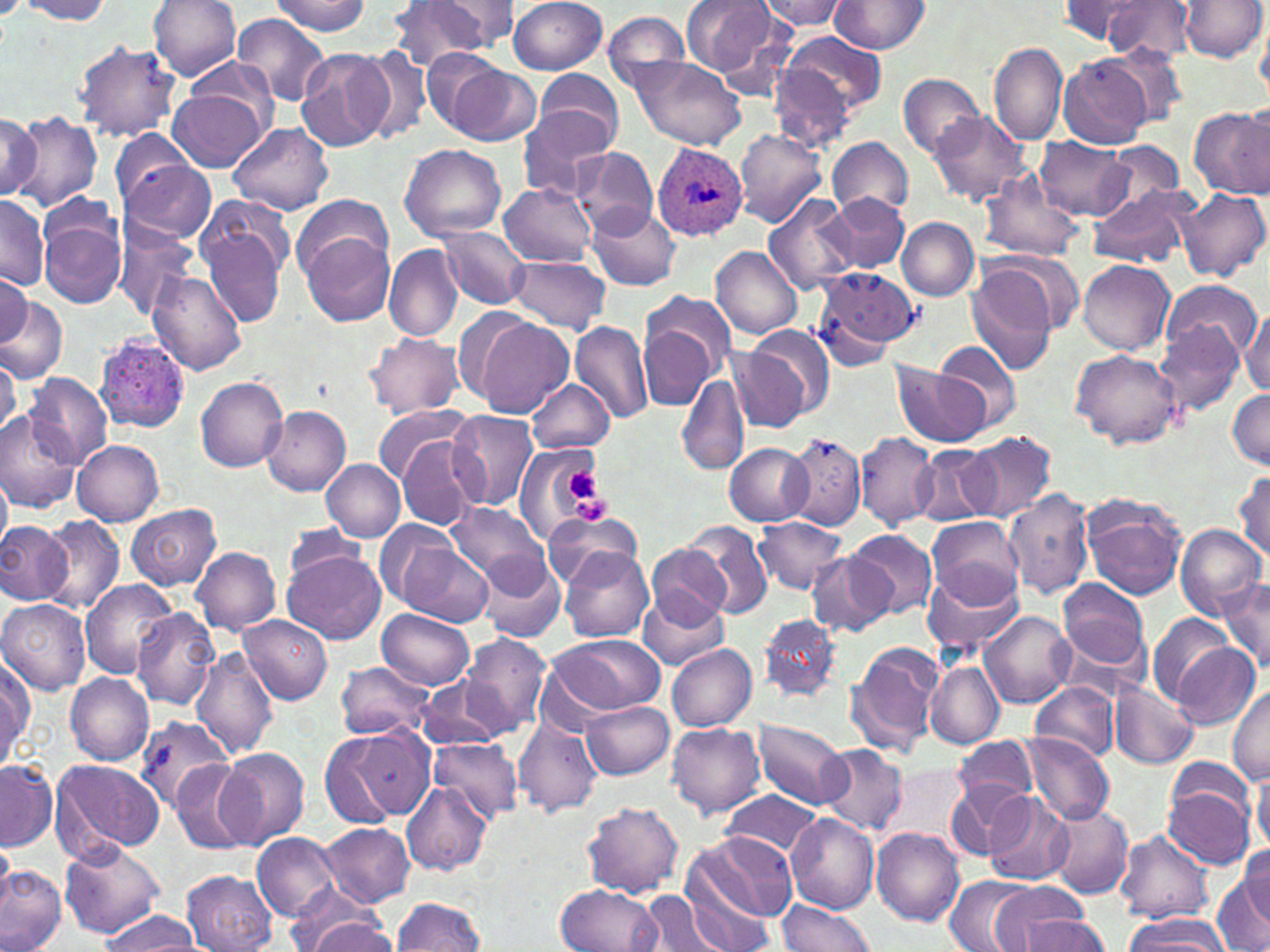
Summary:
  - Coordinate format: approximate bounding boxes as (x1,y1)-(x2,y2) corner pairs in pixels
  - Platelet locations: (564,467)-(612,524)
  - Plasmodium ovale-infected red blood cell locations: (652,143)-(749,240)
  - Uninfected red blood cell locations: (148,0)-(242,81), (272,0)-(372,36), (508,0)-(608,75), (681,0)-(780,79), (830,0)-(929,54), (1103,0)-(1195,64), (1179,0)-(1265,63), (18,1)-(116,25), (757,1)-(850,30), (1055,1)-(1151,47), (386,2)-(494,75), (428,2)-(520,52), (601,9)-(692,94), (233,13)-(330,106), (1256,17)-(1270,102), (257,26)-(366,129), (779,31)-(886,118), (74,41)-(182,143), (989,43)-(1068,148), (1100,43)-(1190,129), (353,45)-(434,146), (295,47)-(391,152), (417,47)-(507,133), (183,56)-(280,133), (632,56)-(747,150), (1059,56)-(1151,149), (439,60)-(539,145), (769,61)-(860,152), (535,69)-(624,151), (898,73)-(984,160), (168,89)-(268,172), (1236,101)-(1268,193), (521,106)-(618,199), (1189,106)-(1270,197), (929,110)-(1032,209), (7,111)-(103,213), (0,113)-(40,199), (229,122)-(334,215), (107,128)-(201,211), (735,128)-(828,227), (828,136)-(913,220), (1037,137)-(1134,222), (1102,142)-(1185,213), (398,143)-(508,240), (570,147)-(658,234), (117,158)-(217,245), (978,174)-(1086,264), (498,183)-(598,267), (1176,186)-(1269,282), (1089,187)-(1196,268), (763,193)-(860,296), (0,194)-(51,291), (293,194)-(393,274), (828,194)-(909,273), (587,204)-(680,291), (196,206)-(293,331), (39,212)-(126,310), (897,218)-(978,301), (111,224)-(199,321), (437,225)-(532,309), (300,231)-(395,327), (383,242)-(464,342), (712,246)-(804,339), (982,252)-(1082,339), (508,255)-(611,334), (1077,260)-(1175,355), (813,266)-(921,361), (966,266)-(1056,375), (147,270)-(247,375), (0,273)-(31,346), (1159,279)-(1262,364), (642,290)-(737,385), (0,296)-(67,383), (1241,307)-(1270,399), (468,313)-(574,418), (640,319)-(718,411), (1153,319)-(1245,416), (569,322)-(654,424), (364,331)-(462,418), (727,332)-(825,433), (94,336)-(189,434), (936,340)-(1022,431), (1071,349)-(1181,449), (892,363)-(989,448), (26,373)-(114,469), (676,373)-(748,474), (197,376)-(289,472), (528,380)-(613,453), (1228,388)-(1270,469), (372,405)-(469,484), (262,406)-(351,496), (0,411)-(81,512), (446,411)-(538,512), (963,431)-(1058,521), (855,432)-(940,533), (395,433)-(484,532), (785,434)-(867,529), (73,440)-(164,526), (725,443)-(814,526), (910,444)-(998,526), (515,445)-(612,543), (321,459)-(405,542), (1232,469)-(1270,566), (0,470)-(11,560), (1005,488)-(1095,600), (1079,496)-(1188,600), (447,503)-(551,589), (126,504)-(221,591), (541,512)-(644,588), (40,514)-(125,615), (927,515)-(1024,608), (753,516)-(849,594), (375,519)-(465,614), (0,520)-(72,606), (685,520)-(772,619), (282,522)-(373,593), (1176,525)-(1266,618), (846,529)-(938,619), (646,545)-(733,626), (399,546)-(495,629), (190,547)-(281,635), (559,548)-(656,642), (283,550)-(385,643), (806,552)-(892,636), (476,554)-(566,643), (922,566)-(1026,657), (1057,577)-(1151,675), (1218,578)-(1270,676), (80,579)-(179,678), (636,594)-(731,671), (0,598)-(91,693), (129,609)-(221,709), (378,609)-(476,690), (981,610)-(1076,709), (758,613)-(842,705), (1147,614)-(1236,705), (237,615)-(332,704), (458,632)-(552,736), (540,634)-(666,720), (844,641)-(944,757), (1167,641)-(1260,729), (666,642)-(757,732), (192,648)-(276,760), (0,650)-(34,766), (925,661)-(1004,748), (333,662)-(436,739), (64,672)-(154,766), (416,678)-(508,751), (1029,680)-(1122,764), (1110,681)-(1198,770), (1229,687)-(1270,784), (581,700)-(675,779), (134,714)-(235,813), (513,715)-(604,818), (753,721)-(852,809), (667,723)-(767,816), (318,725)-(430,829), (516,730)-(629,871), (1022,731)-(1115,826), (430,736)-(524,823), (953,736)-(1039,806), (818,744)-(909,835), (218,749)-(310,849), (51,758)-(164,859), (171,758)-(253,854), (0,760)-(57,851), (880,761)-(971,848), (1251,768)-(1270,853), (1163,770)-(1259,873), (947,778)-(1031,859), (402,780)-(492,876), (719,791)-(824,861), (983,792)-(1074,886), (581,800)-(683,898), (1045,804)-(1133,899), (786,814)-(880,915), (319,823)-(415,907), (872,829)-(963,927), (686,830)-(792,926), (1115,830)-(1213,923), (253,832)-(342,920), (0,835)-(16,916), (61,842)-(165,939), (1236,843)-(1270,927), (0,865)-(65,952), (182,870)-(278,952), (680,874)-(774,952), (1214,874)-(1270,952), (947,875)-(1034,952), (988,882)-(1090,952), (554,883)-(664,951), (637,891)-(729,952), (392,896)-(486,951), (777,900)-(876,952), (292,907)-(397,952), (96,909)-(203,950), (1123,912)-(1232,951), (1012,915)-(1109,952)
  - Slide-level diagnosis: Plasmodium ovale
  - Field of view: single
  - Image size: 1270×952 pixels
  - Magnification: 1000x
  - Preparation: thin blood film
  - Modality: optical microscopy
  - Stain: May-Grünwald-Giemsa